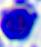
magnification = 400x
identification = leukocyte
modality = photomicrograph